Locate every leukocyte (white blood cell).
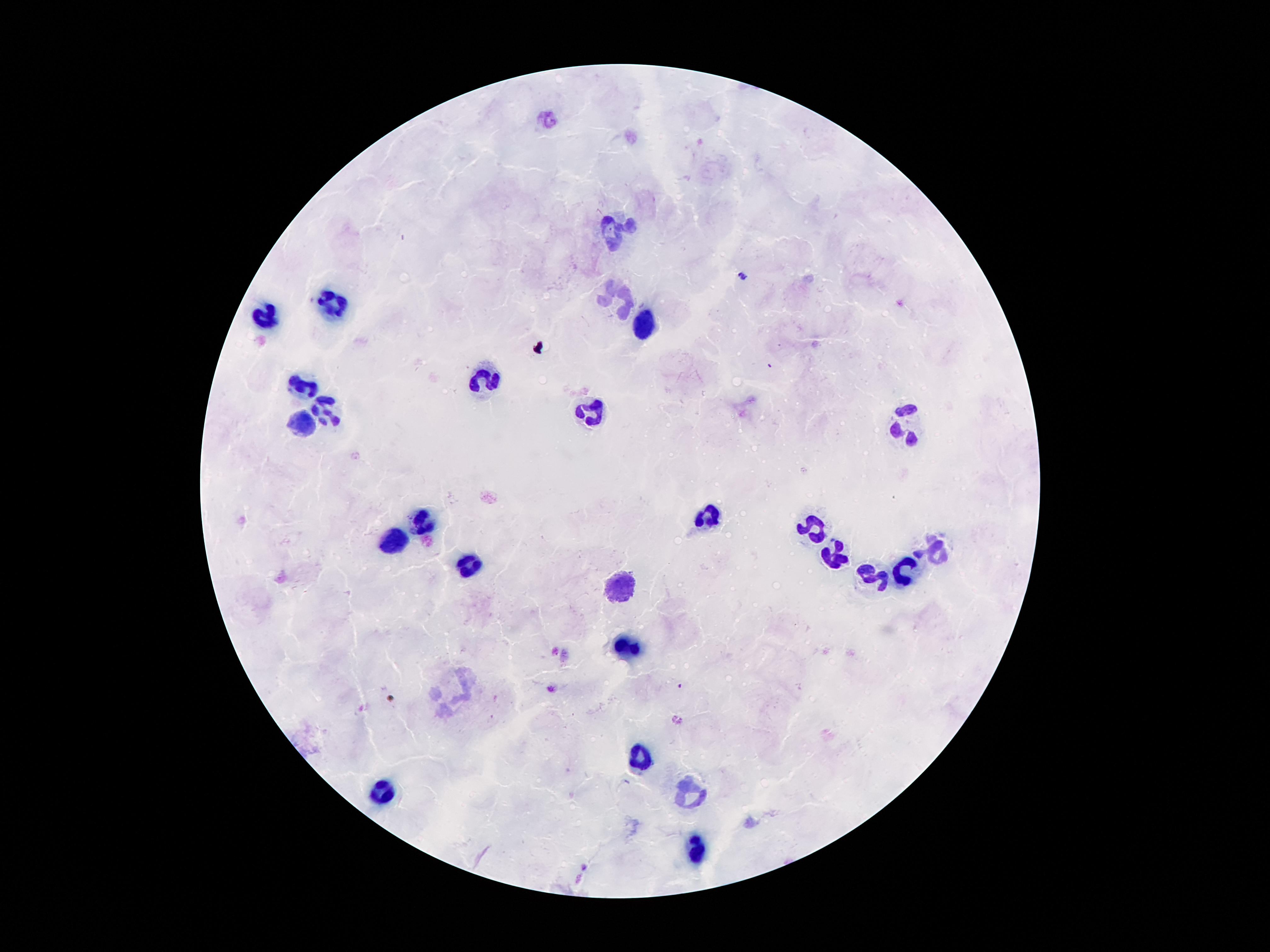

Approximate centers as {x, y} in pixels.
Leukocytes: {612, 232}, {621, 297}, {331, 305}, {262, 319}, {642, 324}, {486, 383}, {300, 388}, {321, 403}, {593, 406}, {906, 425}, {304, 426}, {707, 517}, {423, 520}, {812, 526}, {392, 540}, {936, 550}, {833, 555}, {469, 568}, {906, 570}, {875, 578}, {621, 589}, {629, 646}, {639, 757}, {381, 789}, {688, 789}, {700, 848}.

malaria parasite locations = {741, 276}, {681, 686}
field of view = one from this slide
capture = smartphone through the microscope eyepiece
magnification = 100x
preparation = thick peripheral-blood smear
stain = Giemsa
patient malaria status = infected with Plasmodium falciparum
image size = 1270×952 pixels